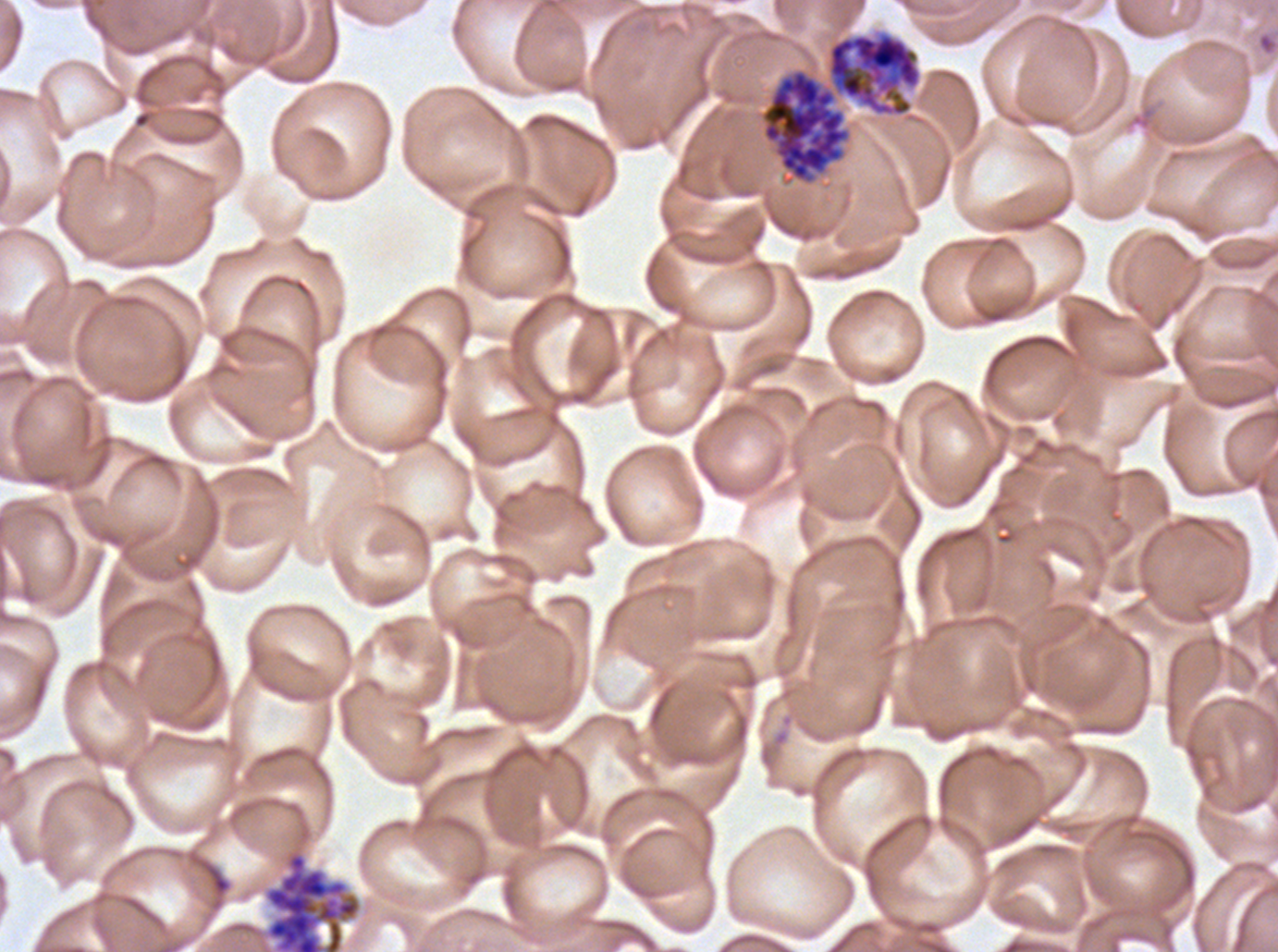 Approximate bounding boxes as {x1, y1, x2, y2} in pixels. Late schizont locations: {760, 31, 922, 184}. Segmenter locations: {263, 848, 363, 951}. One sub-image of a larger composite. Life-cycle stages observed: late schizont, segmenter. Giemsa-stained preparation. Plasmodium falciparum from a patient in The Gambia, cultured ex vivo for 24 to 48 hours. Thin blood smear. Image is 1278×952 pixels.